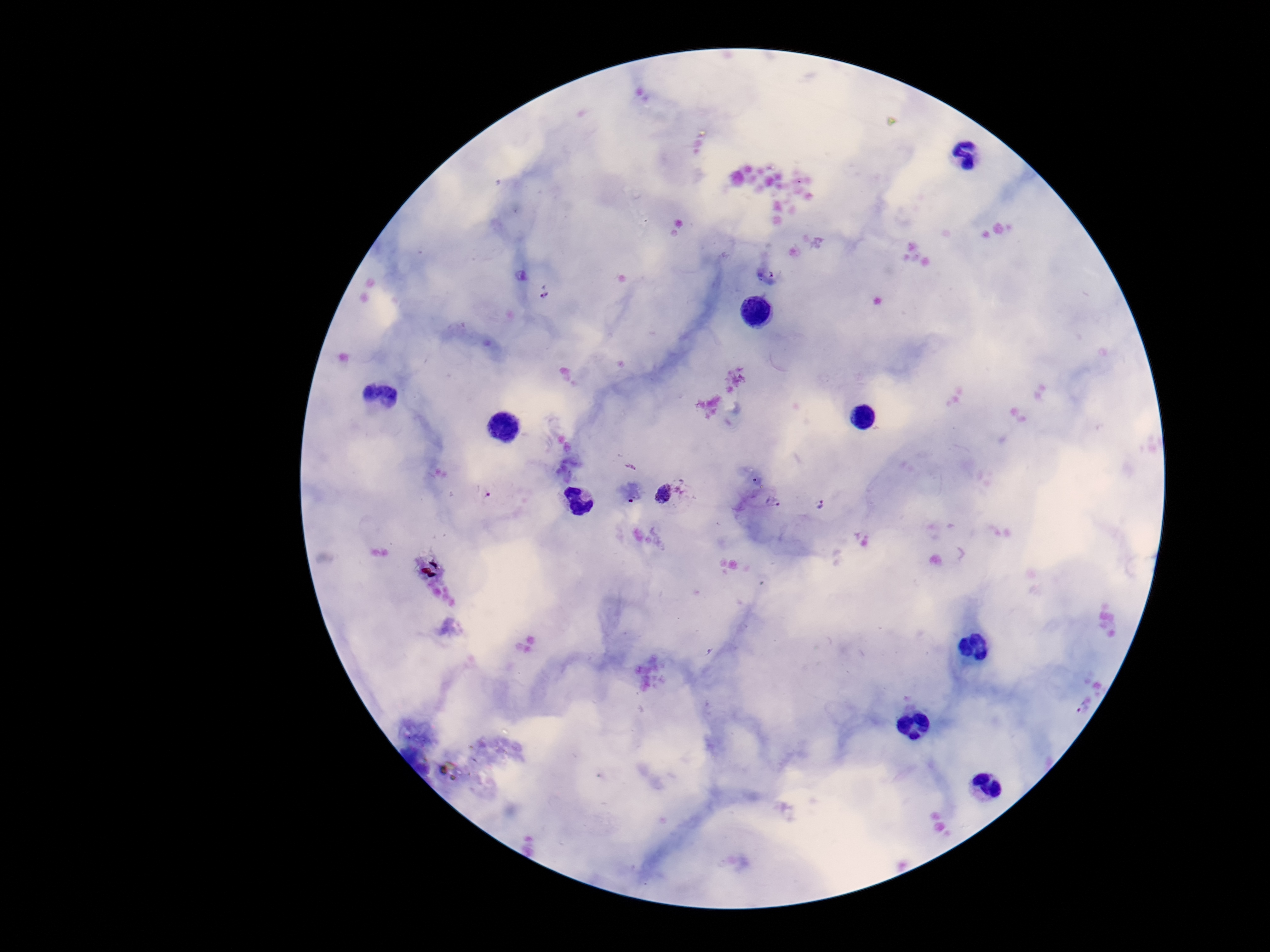

Approximate centers as {x, y} in pixels. Plasmodium parasite locations: {543, 292}, {672, 493}, {484, 495}, {775, 501}, {820, 503}, {1083, 708}. 100x magnification. Single field of view. Patient malaria status: infected. Smartphone photograph taken through the microscope eyepiece. Giemsa-stained preparation. Thick peripheral-blood smear. Image is 1270×952 pixels.